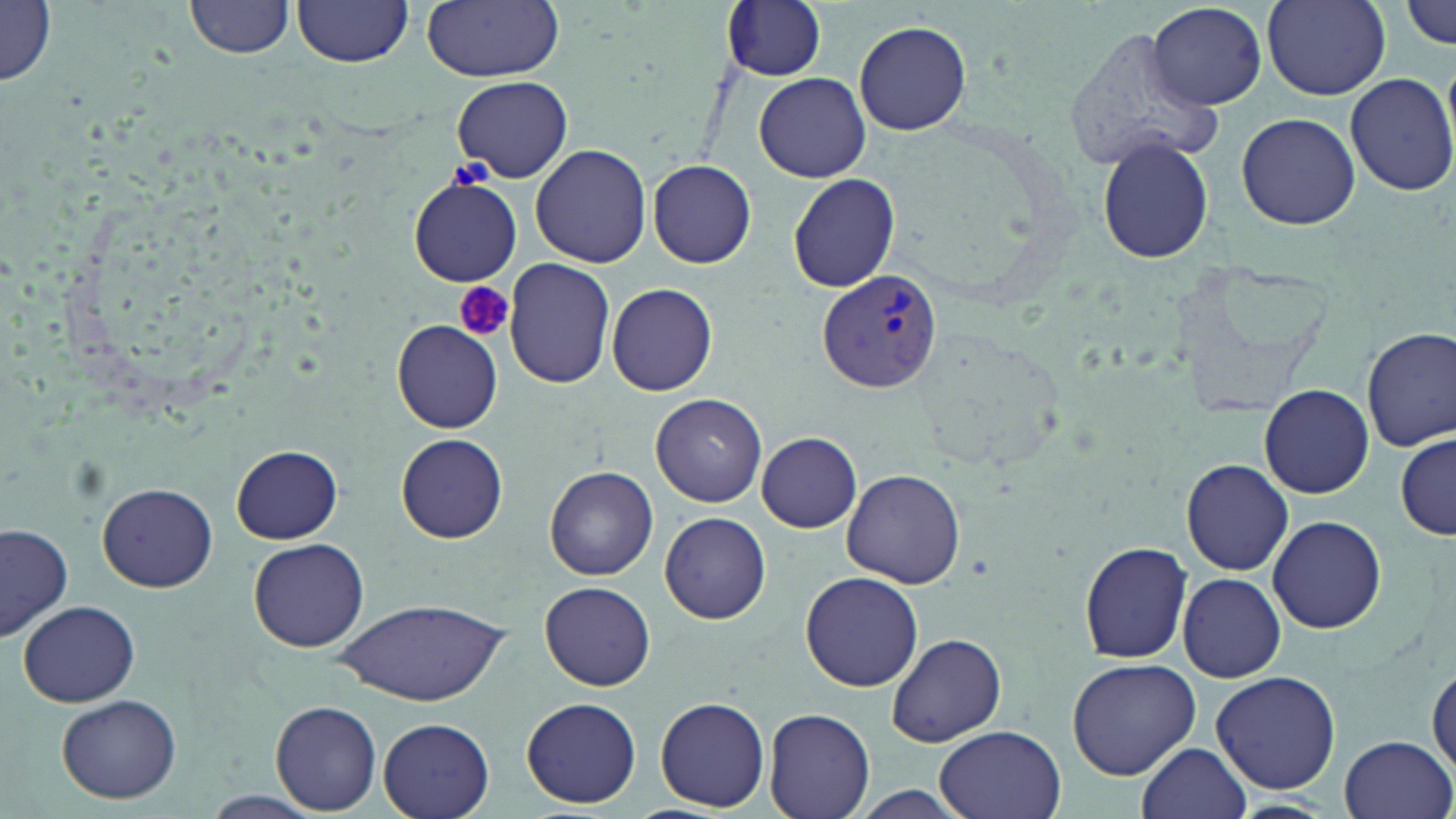

{
  "slide_level_diagnosis": "Plasmodium vivax",
  "field_of_view": "single",
  "uninfected_red_blood_cell_locations": "approximate bounding boxes as [x1, y1, x2, y2] in pixels: [1, 0, 58, 86], [185, 0, 295, 59], [293, 0, 414, 68], [1401, 0, 1456, 50], [423, 1, 565, 82], [721, 1, 828, 82], [1148, 2, 1267, 110], [1263, 2, 1390, 100], [1059, 20, 1219, 178], [854, 21, 971, 134], [1345, 70, 1456, 197], [753, 72, 871, 182], [452, 76, 573, 183], [1233, 111, 1361, 230], [1092, 134, 1215, 265], [530, 142, 652, 267], [647, 158, 757, 268], [787, 173, 901, 293], [407, 178, 520, 287], [503, 258, 615, 389], [607, 283, 718, 397], [392, 319, 503, 433], [1362, 326, 1456, 452], [1258, 384, 1375, 499], [651, 394, 767, 507], [396, 432, 508, 543], [756, 432, 863, 532], [1396, 433, 1455, 540], [232, 444, 343, 543], [1178, 458, 1295, 574], [546, 466, 659, 581], [842, 468, 965, 588], [96, 481, 217, 592], [660, 510, 772, 624], [1266, 514, 1388, 634], [1, 522, 74, 643], [249, 537, 370, 653], [1080, 539, 1195, 664], [801, 571, 924, 691], [1177, 572, 1284, 682], [539, 580, 656, 691], [337, 596, 505, 704], [18, 600, 139, 707], [885, 632, 1005, 749], [1066, 657, 1203, 781], [1428, 658, 1456, 776], [1210, 671, 1340, 794], [56, 694, 181, 802], [522, 696, 641, 808], [655, 696, 771, 811], [271, 701, 382, 815], [764, 708, 877, 819], [377, 718, 494, 819], [934, 725, 1067, 819], [1339, 733, 1454, 818], [1136, 741, 1252, 819], [1224, 798, 1339, 818]",
  "magnification": "1000x",
  "plasmodium_vivax_infected_red_blood_cell_locations": "approximate bounding boxes as [x1, y1, x2, y2] in pixels: [818, 267, 943, 395]",
  "platelet_locations": "approximate bounding boxes as [x1, y1, x2, y2] in pixels: [455, 283, 515, 342]",
  "modality": "optical microscopy",
  "stain": "May-Grünwald-Giemsa",
  "image_size": "1456×819 pixels",
  "preparation": "thin blood smear"
}